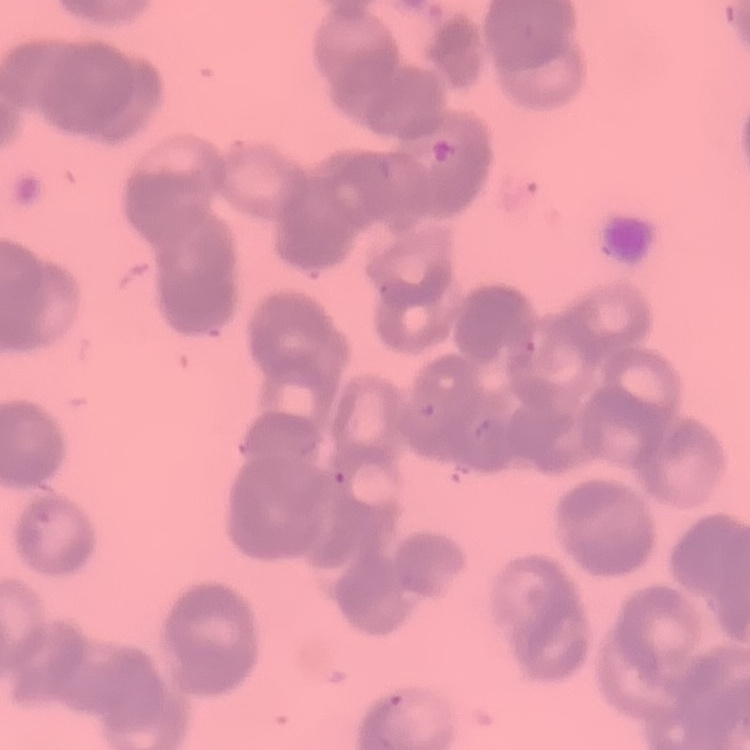

The erythrocytes exhibit rouleaux formation. Field's or Giemsa stain. Thin blood film. Square crop of a larger photomicrograph.